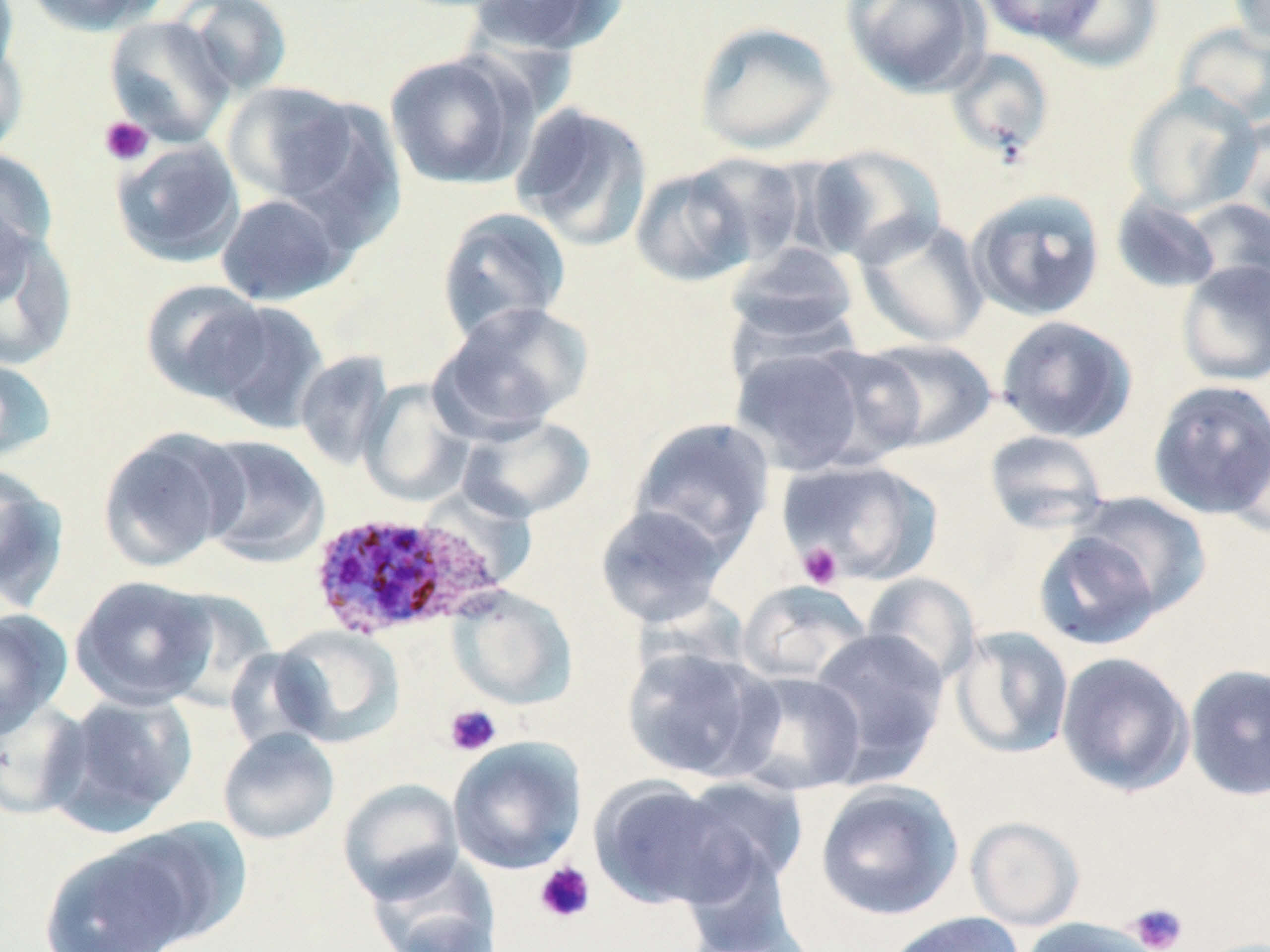

Approximate bounding boxes as (x1, y1, x2, y2) in pixels. Uninfected red blood cell locations: (0, 0, 20, 82), (22, 0, 167, 37), (176, 0, 294, 98), (467, 0, 626, 57), (840, 0, 989, 98), (976, 0, 1106, 44), (1039, 0, 1163, 73), (1229, 0, 1270, 46), (103, 15, 235, 147), (693, 19, 839, 156), (1173, 23, 1270, 132), (0, 37, 28, 160), (943, 48, 1056, 163), (385, 52, 532, 190), (221, 81, 360, 204), (1126, 84, 1262, 217), (510, 102, 654, 250), (1229, 114, 1270, 235), (111, 138, 245, 267), (805, 144, 948, 268), (0, 147, 59, 271), (684, 152, 812, 270), (630, 165, 760, 288), (966, 187, 1106, 321), (216, 192, 349, 306), (1110, 194, 1222, 294), (1184, 198, 1269, 299), (436, 206, 572, 343), (854, 215, 989, 349), (0, 223, 77, 373), (725, 243, 860, 345), (1176, 260, 1270, 386), (139, 279, 272, 404), (432, 300, 594, 438), (203, 301, 329, 433), (996, 315, 1138, 443), (858, 338, 998, 454), (728, 344, 882, 475), (801, 345, 931, 468), (295, 350, 395, 471), (0, 356, 57, 463), (358, 377, 476, 507), (1147, 378, 1270, 520), (456, 414, 597, 523), (628, 416, 775, 557), (1221, 419, 1270, 540), (97, 428, 244, 573), (983, 430, 1110, 535), (195, 435, 331, 567), (781, 458, 944, 585), (0, 466, 69, 613), (1072, 491, 1212, 618), (594, 504, 732, 628), (1032, 529, 1162, 651), (861, 572, 982, 689), (69, 575, 219, 710), (736, 580, 872, 686), (445, 586, 578, 711), (0, 609, 72, 738), (268, 625, 404, 747), (950, 626, 1075, 760), (808, 628, 950, 782), (620, 643, 777, 783), (1055, 651, 1195, 798), (1184, 662, 1270, 802), (730, 671, 867, 796), (46, 690, 199, 836), (0, 696, 92, 821), (217, 728, 340, 845), (448, 736, 586, 875), (674, 776, 809, 897), (589, 777, 740, 911), (338, 778, 465, 903), (815, 779, 964, 921), (966, 816, 1084, 931), (113, 817, 251, 949), (38, 838, 197, 952), (364, 853, 502, 952), (879, 912, 1025, 952), (1018, 917, 1162, 952). Plasmodium ovale-infected red blood cell locations: (306, 511, 506, 641). Platelet locations: (99, 116, 154, 166), (797, 542, 843, 589), (444, 703, 502, 757), (533, 861, 596, 924), (1127, 902, 1188, 952). Slide-level diagnosis: Plasmodium ovale. 1000x magnification. Thin blood film. Optical microscopy. Image is 1270×952 pixels. May-Grünwald-Giemsa-stained preparation. One field of a larger specimen.